Outline each uninfected red blood cell.
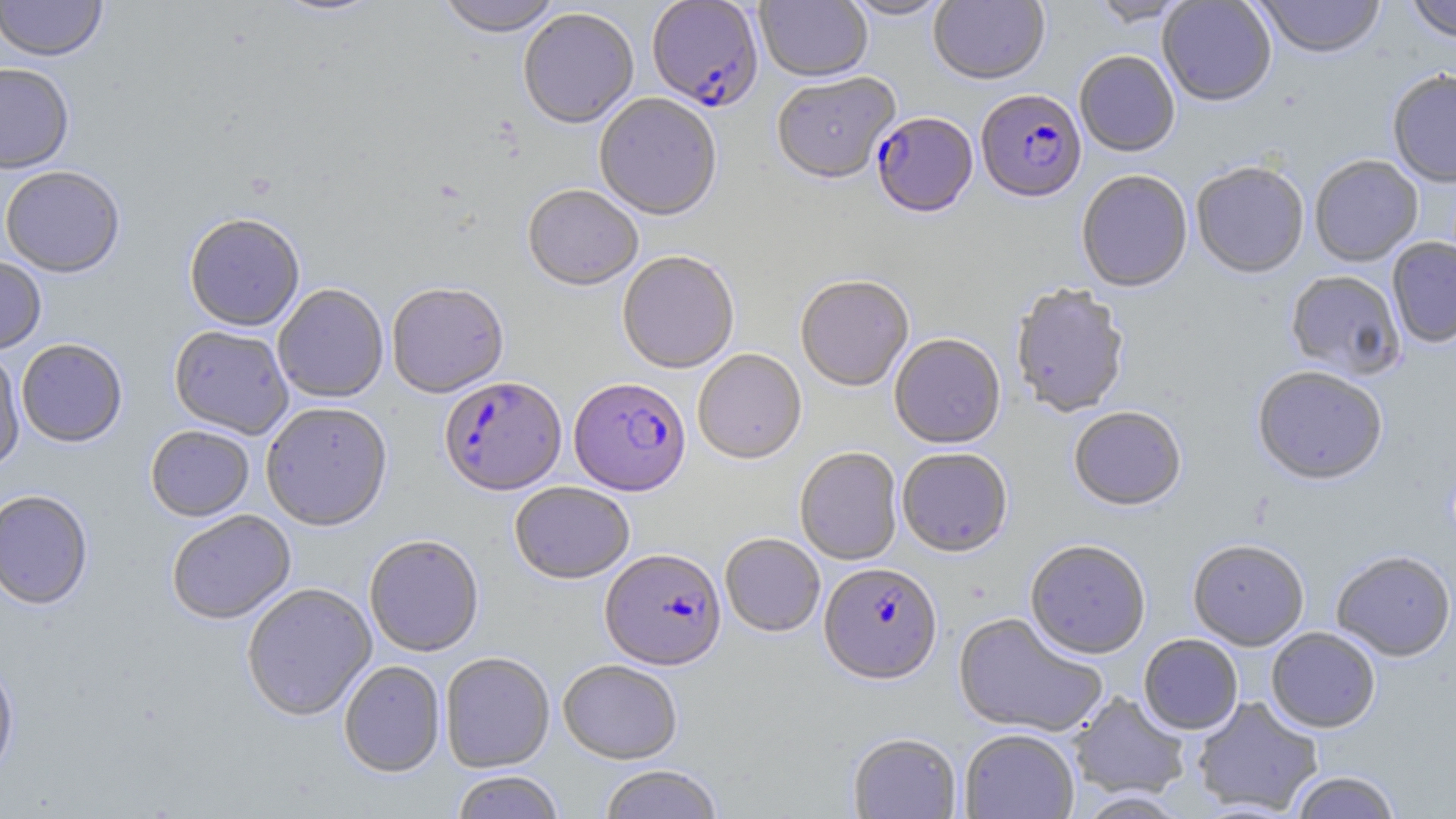
Approximate bounding boxes as [x1, y1, x2, y2] in pixels.
Uninfected red blood cells: [0, 0, 107, 62], [270, 0, 386, 20], [435, 0, 562, 40], [756, 0, 872, 84], [840, 0, 953, 21], [929, 0, 1050, 88], [1089, 0, 1194, 28], [1254, 0, 1387, 61], [1405, 0, 1456, 44], [1158, 1, 1276, 108], [519, 10, 638, 131], [1074, 53, 1180, 159], [0, 62, 75, 175], [1387, 70, 1456, 189], [772, 74, 901, 187], [594, 95, 722, 223], [1310, 156, 1423, 268], [1191, 164, 1309, 280], [0, 166, 125, 278], [1076, 171, 1192, 295], [522, 187, 642, 293], [184, 216, 304, 333], [1387, 238, 1456, 349], [617, 253, 740, 376], [0, 256, 47, 355], [1285, 272, 1405, 381], [795, 278, 914, 393], [387, 284, 509, 399], [273, 285, 389, 404], [1010, 285, 1130, 420], [168, 326, 293, 440], [889, 336, 1006, 451], [16, 340, 127, 449], [0, 350, 25, 473], [693, 350, 807, 466], [1252, 368, 1387, 488], [261, 404, 392, 532], [1068, 408, 1187, 513], [145, 427, 254, 522], [794, 448, 903, 567], [897, 450, 1013, 559], [510, 483, 635, 586], [0, 490, 93, 611], [167, 511, 296, 626], [720, 534, 825, 638], [365, 535, 484, 659], [1188, 541, 1309, 651], [1025, 542, 1151, 661], [1331, 552, 1455, 663], [242, 584, 377, 723], [953, 613, 1107, 739], [1266, 628, 1380, 734], [1139, 635, 1243, 736], [440, 653, 555, 774], [0, 656, 19, 784], [338, 661, 445, 778], [558, 661, 682, 766], [1069, 692, 1190, 799], [1192, 696, 1323, 815], [960, 729, 1079, 819], [847, 733, 962, 819], [599, 766, 723, 819], [451, 772, 564, 819], [1289, 772, 1401, 819], [1073, 792, 1193, 818].

Summary:
  - Plasmodium falciparum-infected red blood cell locations: [646, 0, 763, 115], [976, 91, 1086, 205], [871, 114, 977, 220], [439, 378, 566, 497], [569, 380, 691, 498], [601, 550, 726, 672], [819, 564, 943, 687]
  - Slide-level diagnosis: Plasmodium falciparum
  - Modality: optical microscopy
  - Magnification: 1000x
  - Image size: 1456×819 pixels
  - Stain: May-Grünwald-Giemsa
  - Preparation: thin blood smear
  - Field of view: one of a larger specimen